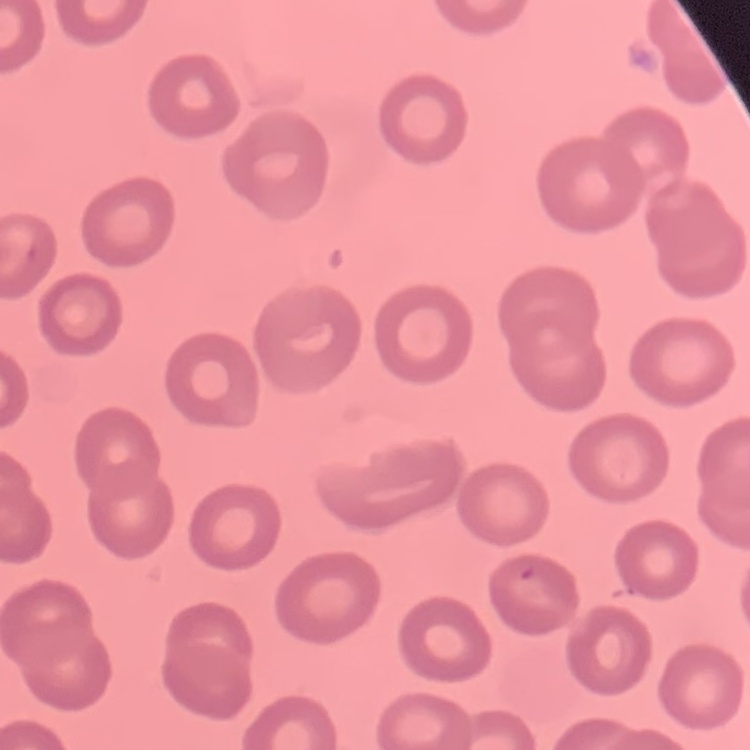
The red blood cells show no rouleaux formation. One tile cut from a larger photomicrograph. Stained with either Field's or Giemsa. Thin peripheral smear.